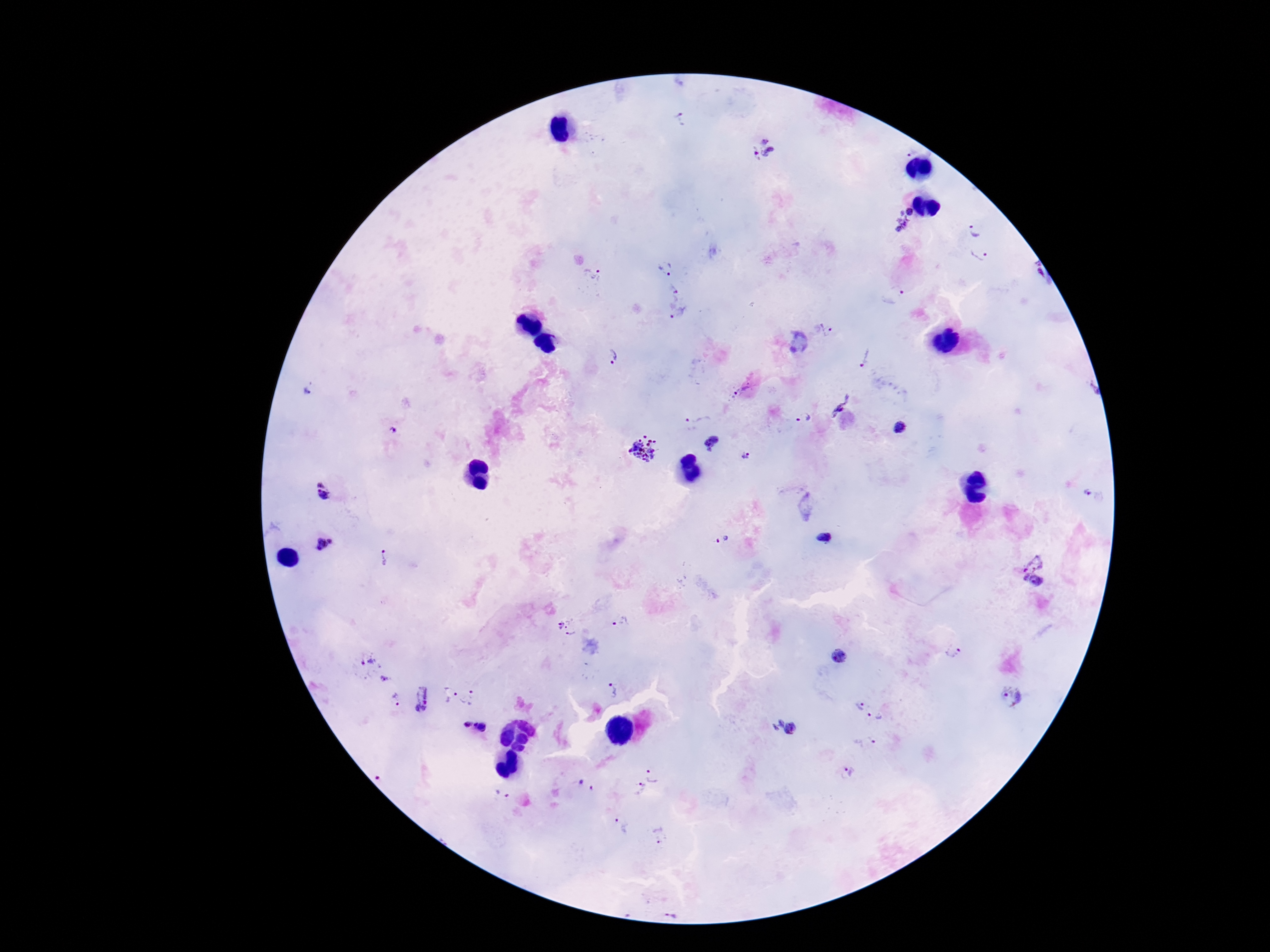
Approximate centers as {x, y} in pixels.
Summary:
  - Plasmodium parasite locations: {680, 118}, {763, 149}, {912, 212}, {894, 222}, {974, 230}, {980, 255}, {666, 268}, {591, 276}, {674, 289}, {895, 295}, {678, 312}, {828, 331}, {609, 356}, {863, 357}, {310, 389}, {742, 391}, {842, 407}, {804, 418}, {697, 423}, {900, 426}, {393, 431}, {711, 441}, {644, 449}, {746, 456}, {326, 491}, {1089, 492}, {823, 538}, {723, 540}, {323, 544}, {384, 556}, {1033, 560}, {1032, 588}, {620, 622}, {568, 627}, {953, 651}, {840, 656}, {367, 664}, {386, 680}, {612, 690}, {447, 694}, {472, 697}, {1010, 697}, {421, 699}, {392, 700}, {857, 706}, {877, 717}, {466, 724}, {481, 727}, {786, 728}, {872, 740}, {848, 771}, {657, 772}, {382, 777}, {590, 783}, {635, 788}, {504, 792}, {621, 825}, {658, 833}
  - Capture: smartphone camera through the microscope eyepiece
  - Field of view: single
  - Preparation: thick peripheral-blood smear
  - Magnification: 100x
  - Stain: Giemsa
  - Patient malaria status: positive
  - Image size: 1270×952 pixels